Classify this cell by malaria status.
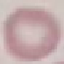

It is uninfected.

preparation = thin smear
stain = Giemsa
capture = smartphone camera at the microscope eyepiece
image type = automatically extracted cell patch, resized to 64 × 64 pixels